State which cell type is depicted.
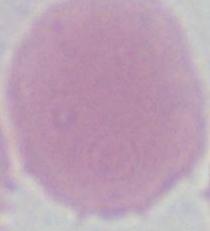

This is an erythrocyte.

Summary:
  - Modality: micrograph
  - Magnification: 1000x